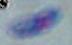

Summary:
  - Modality: photomicrograph
  - Magnification: 1000x
  - Identification: Toxoplasma gondii